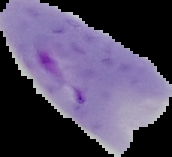
malaria status = parasitized
image size = 172×157 pixels
image type = segmented cell region with the area outside set to black
preparation = thin blood smear